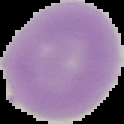

preparation = thin blood film
result = no malaria parasites detected
image type = cell region segmented out of the field of view; surrounding area masked to black
image size = 124×124 pixels